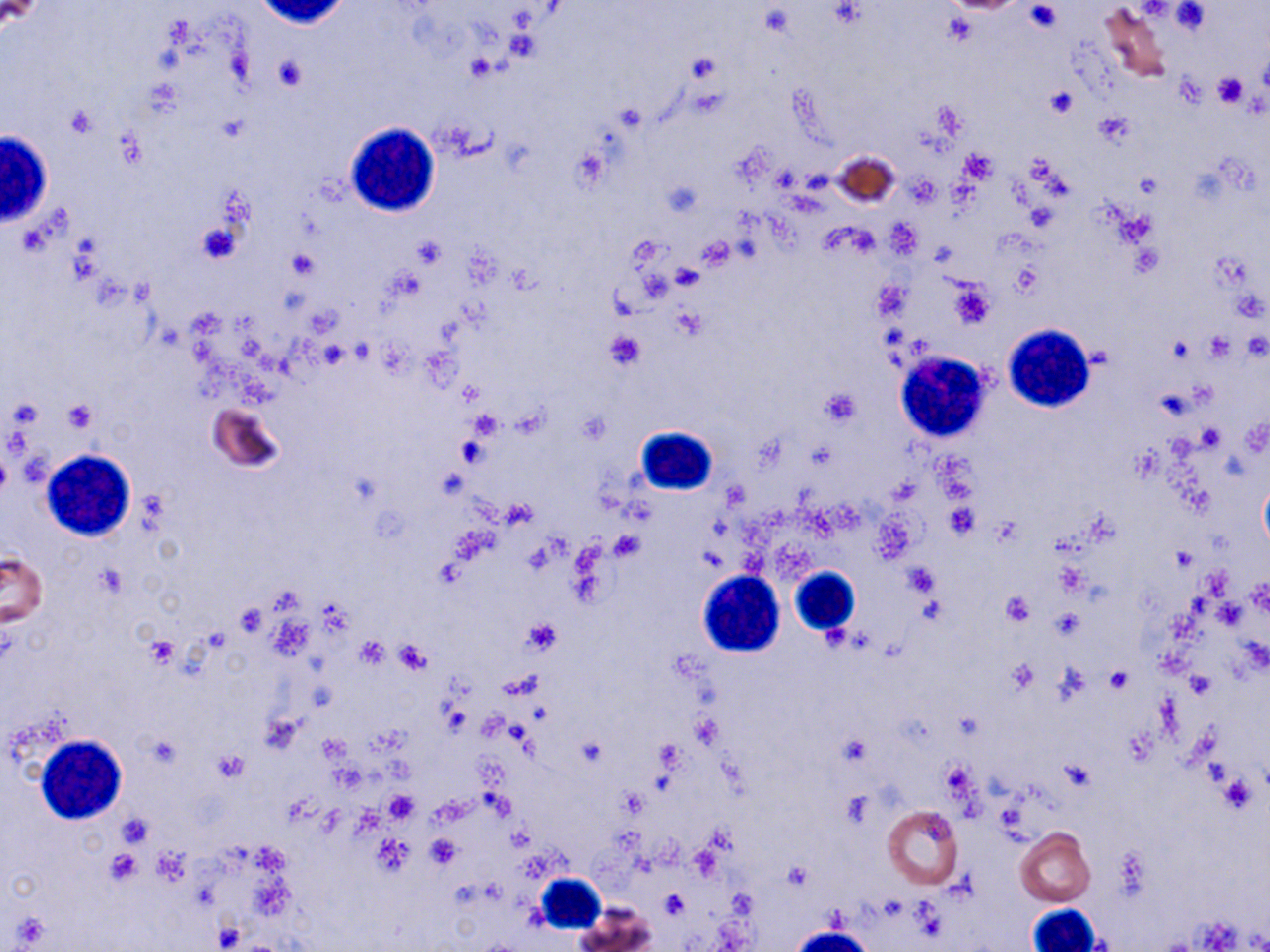
Approximate bounding boxes as (x1, y1, x2, y2) in pixels. Uninfected red blood cell locations: (1098, 4, 1171, 82), (831, 151, 903, 208), (209, 403, 282, 473), (0, 553, 47, 626), (882, 804, 964, 889), (1015, 827, 1096, 906), (576, 906, 655, 952). White blood cell locations: (347, 128, 442, 218), (0, 130, 61, 234), (1004, 324, 1094, 412), (895, 351, 993, 442), (638, 425, 723, 499), (41, 450, 137, 542), (788, 565, 859, 635), (698, 570, 784, 658), (36, 735, 126, 824), (533, 873, 606, 934), (1023, 904, 1102, 952), (788, 927, 877, 952). Platelet locations: (1025, 2, 1061, 32), (1171, 2, 1212, 36), (684, 50, 723, 88), (464, 54, 499, 83), (274, 56, 307, 91), (1211, 73, 1247, 108), (1176, 75, 1208, 108), (1043, 86, 1079, 119), (65, 105, 98, 139), (1095, 114, 1133, 147), (570, 145, 611, 193), (960, 149, 996, 181), (909, 176, 939, 207), (661, 180, 702, 217), (1116, 210, 1157, 247), (196, 222, 242, 264), (412, 236, 445, 271), (698, 238, 733, 270), (1130, 245, 1164, 277), (287, 250, 319, 280), (670, 264, 704, 290), (948, 277, 994, 329), (604, 330, 642, 368), (1203, 333, 1235, 361), (1166, 338, 1192, 364), (819, 386, 863, 427), (61, 398, 100, 433), (465, 410, 505, 443), (1196, 424, 1225, 451), (456, 435, 491, 468), (0, 448, 11, 501), (502, 498, 536, 526), (945, 502, 979, 538), (609, 531, 644, 561), (1172, 547, 1196, 572), (901, 563, 941, 598), (96, 564, 127, 598), (1000, 591, 1034, 626), (234, 602, 268, 635), (521, 617, 562, 656), (145, 637, 178, 667), (357, 638, 387, 670), (394, 640, 430, 673), (1104, 666, 1132, 693), (1188, 672, 1215, 699), (440, 703, 470, 736), (838, 733, 871, 767), (145, 734, 182, 770), (576, 735, 607, 769), (214, 750, 248, 782), (383, 790, 415, 823), (116, 812, 155, 848), (425, 836, 461, 867), (104, 852, 142, 884), (784, 860, 812, 890), (659, 888, 688, 919). Slide-level diagnosis: no evidence of blood parasites. Captured at 1000x magnification. Image is 1270×952 pixels. Thin blood film. One field of a larger specimen. Optical microscopy. May-Grünwald-Giemsa stain.